Point out each Plasmodium parasite.
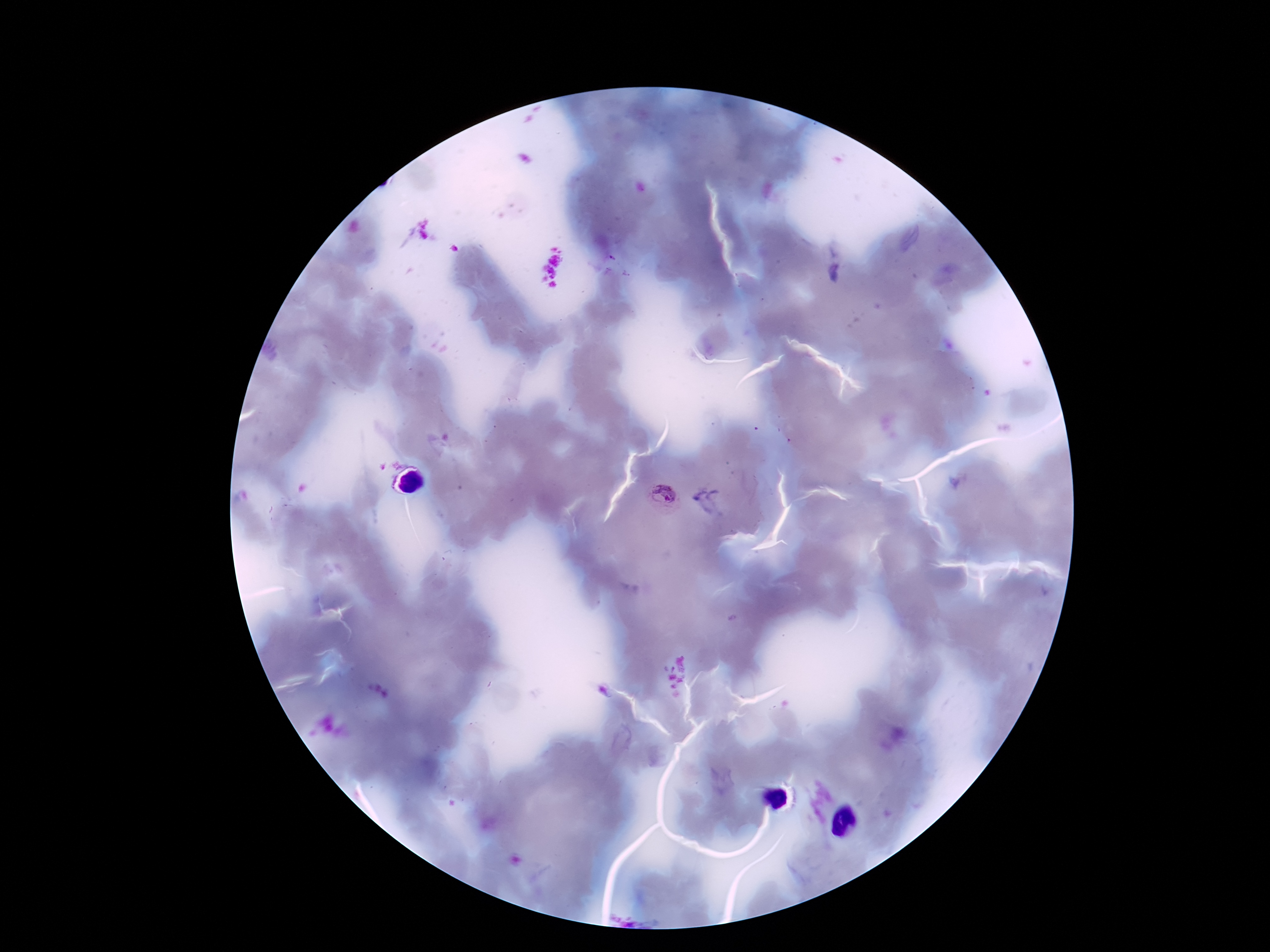
Approximate centers as [x, y] in pixels.
Plasmodium parasites: [665, 495].

100x magnification. Thick blood smear. Photographed through the microscope eyepiece with a smartphone camera. Image is 1270×952 pixels. One field from this slide. Patient malaria status: infected. Giemsa-stained preparation.